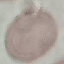
Malaria status: uninfected. Acquired by smartphone through the microscope eyepiece. Automatically extracted cell patch, resized to 64 × 64 pixels. Giemsa stain. Thin smear of blood.